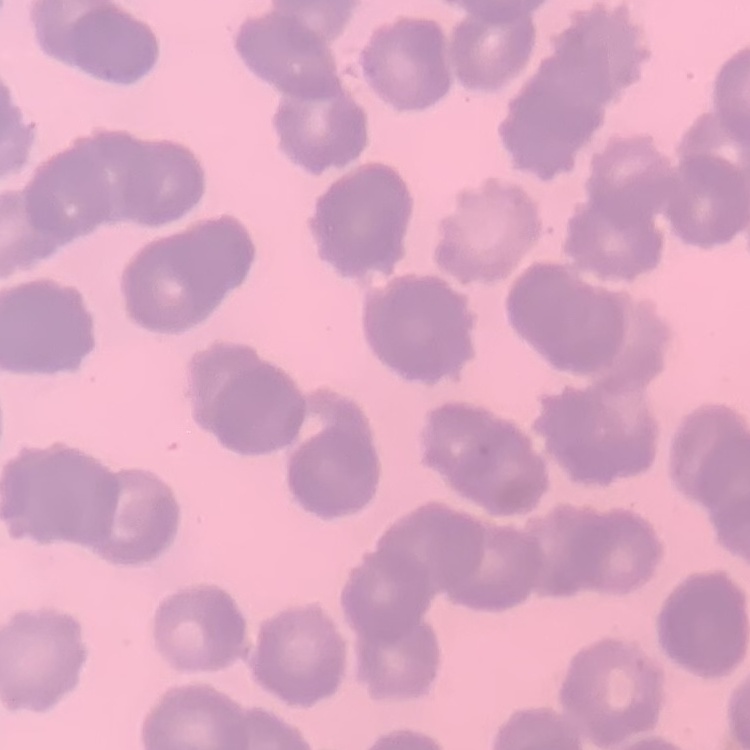
Summary:
  - Erythrocyte morphology: rouleaux formation
  - Preparation: thin peripheral smear
  - Image type: one tile cut from a larger photomicrograph
  - Stain: Field's or Giemsa